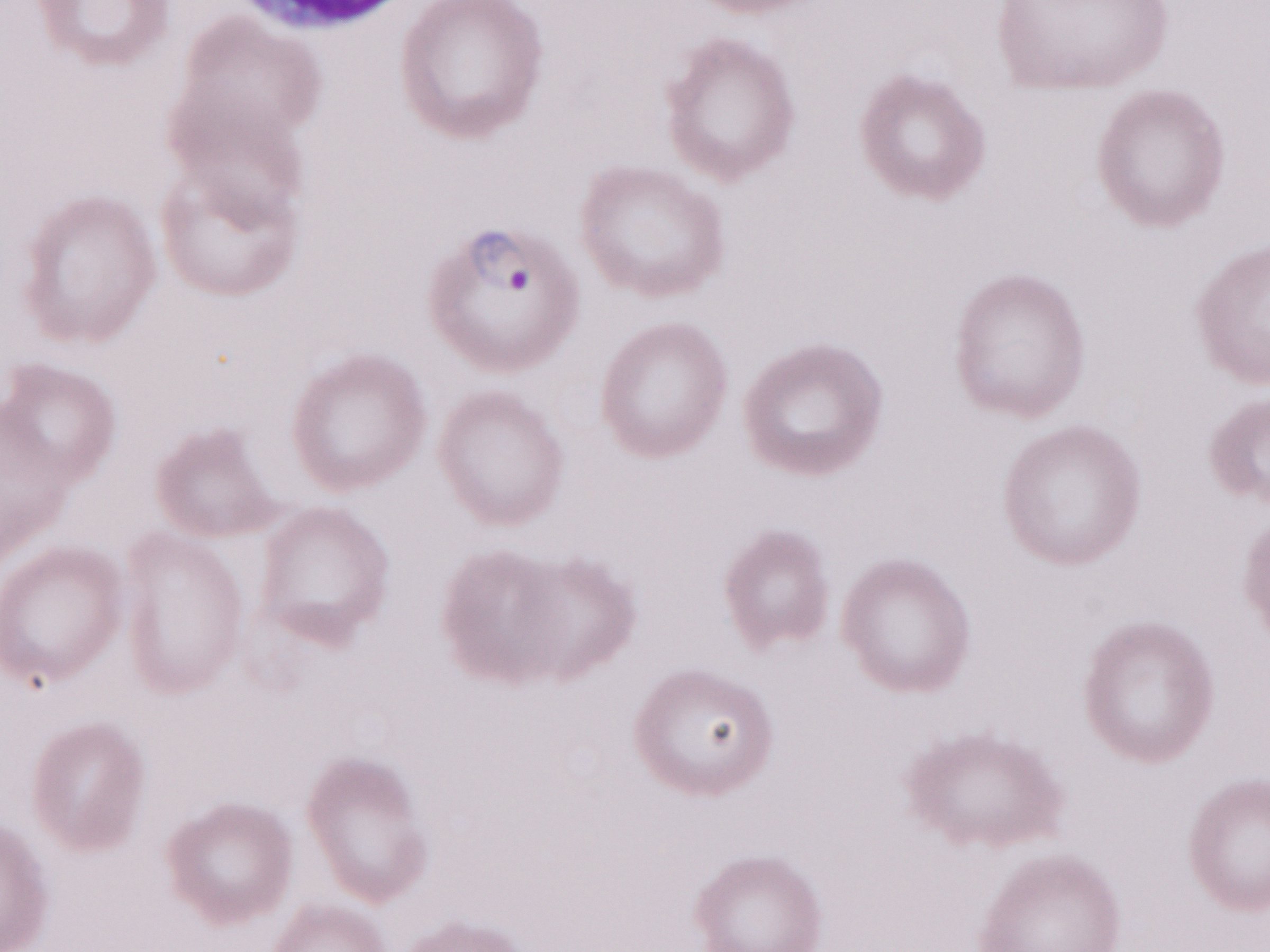
May-Grünwald-Giemsa (MGG) stain. Malaria diagnosis (patient-level): positive. Single field of view. Image is 1270×952 pixels. Olympus BX43 microscope and DP73 digital camera. Thin blood film. Magnification: 1,000x.